Comment on the morphology of the red blood cells.
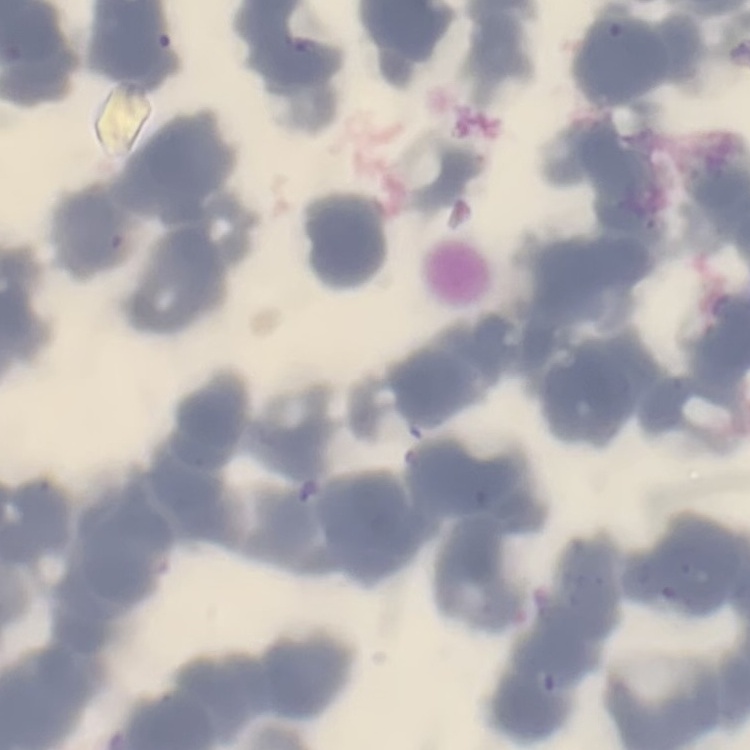

They show rouleaux formation.

image type = one tile cut from a larger photomicrograph
preparation = thin blood film
stain = Field's or Giemsa